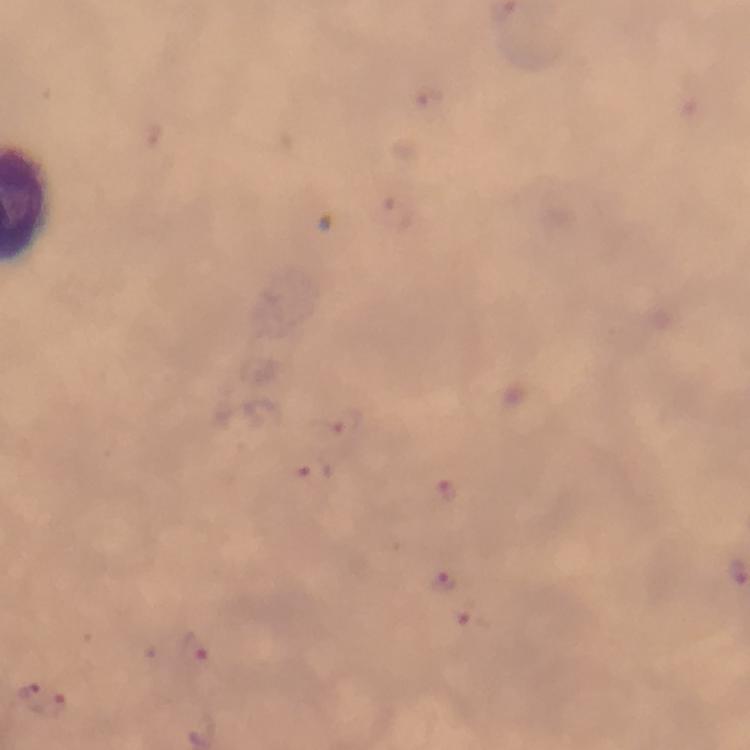 Approximate centers as {x, y} in pixels. Malaria parasite locations: {347, 421}, {318, 472}, {447, 494}, {444, 582}, {473, 620}, {193, 648}, {26, 687}, {53, 704}. From a malaria diagnostic workup. Thick smear. Giemsa-stained preparation. Image is 750×750 pixels. Photographed through the microscope with a smartphone camera. Cropped region of a single field of view. 100x magnification. Immersion oil applied.